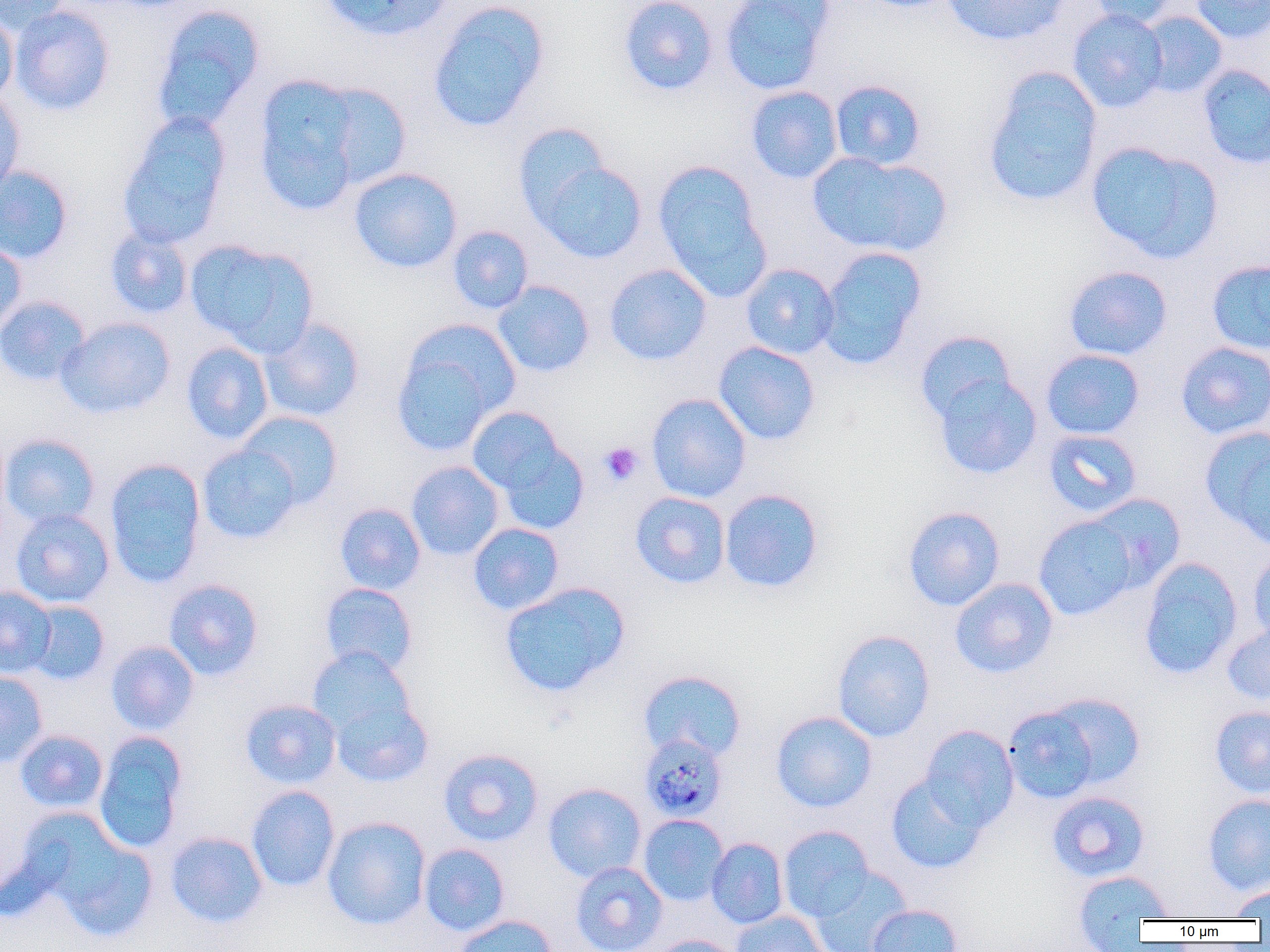
Summary:
  - Coordinate format: approximate bounding boxes as [x1, y1, x2, y2] in pixels
  - Uninfected red blood cell locations: [0, 0, 73, 36], [319, 0, 453, 41], [618, 0, 718, 96], [720, 0, 836, 95], [859, 0, 959, 12], [940, 0, 1071, 47], [1086, 0, 1183, 28], [1190, 0, 1269, 44], [426, 1, 550, 133], [150, 4, 266, 133], [10, 5, 116, 115], [1068, 8, 1169, 113], [0, 10, 18, 105], [1137, 11, 1228, 98], [1198, 65, 1270, 169], [982, 67, 1103, 208], [253, 73, 379, 215], [830, 80, 926, 170], [314, 82, 412, 190], [745, 85, 843, 184], [0, 91, 25, 199], [117, 111, 232, 250], [511, 121, 615, 228], [1086, 141, 1222, 264], [807, 152, 952, 258], [532, 157, 647, 264], [653, 161, 771, 298], [0, 165, 73, 264], [348, 167, 463, 273], [447, 225, 533, 314], [104, 227, 194, 319], [0, 237, 28, 334], [185, 238, 318, 355], [817, 247, 927, 369], [1206, 259, 1270, 354], [741, 263, 840, 359], [604, 264, 712, 366], [1063, 265, 1173, 361], [492, 280, 595, 378], [0, 295, 91, 387], [56, 317, 175, 419], [259, 317, 366, 422], [391, 323, 515, 455], [914, 330, 1016, 424], [180, 341, 273, 444], [713, 341, 820, 445], [1175, 341, 1270, 440], [1041, 349, 1145, 439], [933, 372, 1042, 479], [646, 393, 751, 502], [467, 406, 576, 514], [238, 411, 343, 509], [1200, 426, 1270, 546], [0, 429, 10, 534], [1043, 429, 1142, 518], [1, 433, 101, 528], [197, 444, 302, 544], [104, 457, 207, 587], [406, 461, 505, 560], [719, 488, 824, 593], [630, 491, 731, 589], [1086, 493, 1185, 590], [334, 502, 426, 595], [902, 505, 1005, 611], [10, 509, 114, 607], [1033, 514, 1140, 621], [468, 522, 565, 615], [1247, 548, 1270, 645], [1138, 557, 1243, 680], [163, 578, 264, 680], [949, 578, 1058, 678], [499, 582, 629, 698], [319, 583, 418, 676], [0, 586, 57, 677], [25, 600, 110, 685], [1222, 621, 1270, 707], [832, 629, 936, 742], [105, 640, 200, 735], [306, 646, 416, 743], [637, 669, 747, 762], [0, 671, 49, 767], [1043, 692, 1147, 789], [328, 696, 433, 787], [239, 698, 341, 789], [1209, 705, 1270, 798], [1003, 706, 1101, 803], [771, 710, 877, 812], [920, 724, 1019, 830], [14, 729, 108, 813], [93, 731, 189, 853], [438, 748, 544, 847], [885, 772, 989, 874], [543, 782, 647, 883], [246, 785, 340, 892], [1046, 791, 1151, 882], [1202, 793, 1270, 894], [638, 814, 729, 906], [29, 815, 159, 943], [322, 816, 431, 930], [777, 825, 875, 921], [165, 831, 268, 929], [706, 837, 788, 928], [419, 843, 510, 936], [570, 861, 668, 952], [810, 868, 913, 952], [1072, 869, 1174, 942], [1228, 885, 1270, 920], [866, 904, 963, 952], [730, 910, 829, 952], [451, 914, 558, 952], [650, 935, 745, 952]
  - Platelet locations: [599, 442, 643, 486]
  - Plasmodium malariae-infected red blood cell locations: [641, 737, 723, 815]
  - Slide-level diagnosis: Plasmodium malariae
  - Image size: 1270×952 pixels
  - Magnification: 1000x
  - Modality: light microscopy
  - Preparation: thin blood smear
  - Field of view: one of a larger specimen